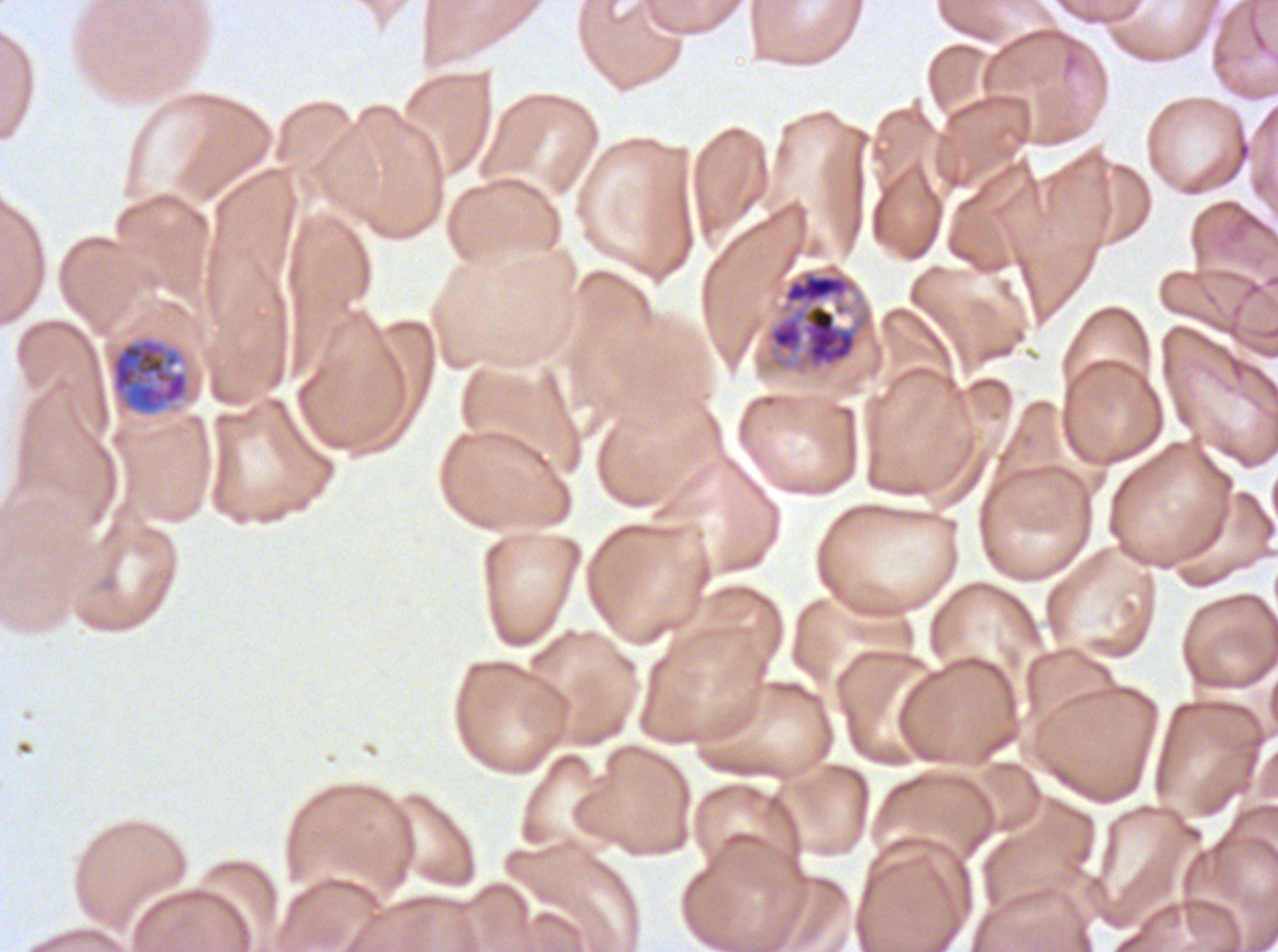
notation = approximate bounding rectangles given as corner coordinates in pixels from the top-left
early schizont locations = (x1=764, y1=262, x2=874, y2=375), (x1=108, y1=335, x2=190, y2=417)
stain = Giemsa
image size = 1278×952 pixels
specimen = ex-vivo P. falciparum culture from a patient in The Gambia, grown for 24 to 48 hours
preparation = thin blood smear
field of view = sub-image separated from a larger composite